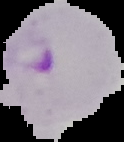
Summary:
  - Result: malaria parasites detected
  - Image size: 124×142 pixels
  - Image type: cell region segmented out of the field of view; surrounding area masked to black
  - Preparation: thin blood film